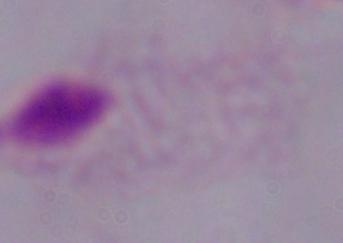

modality = micrograph
magnification = 1000x
identification = trichomonad